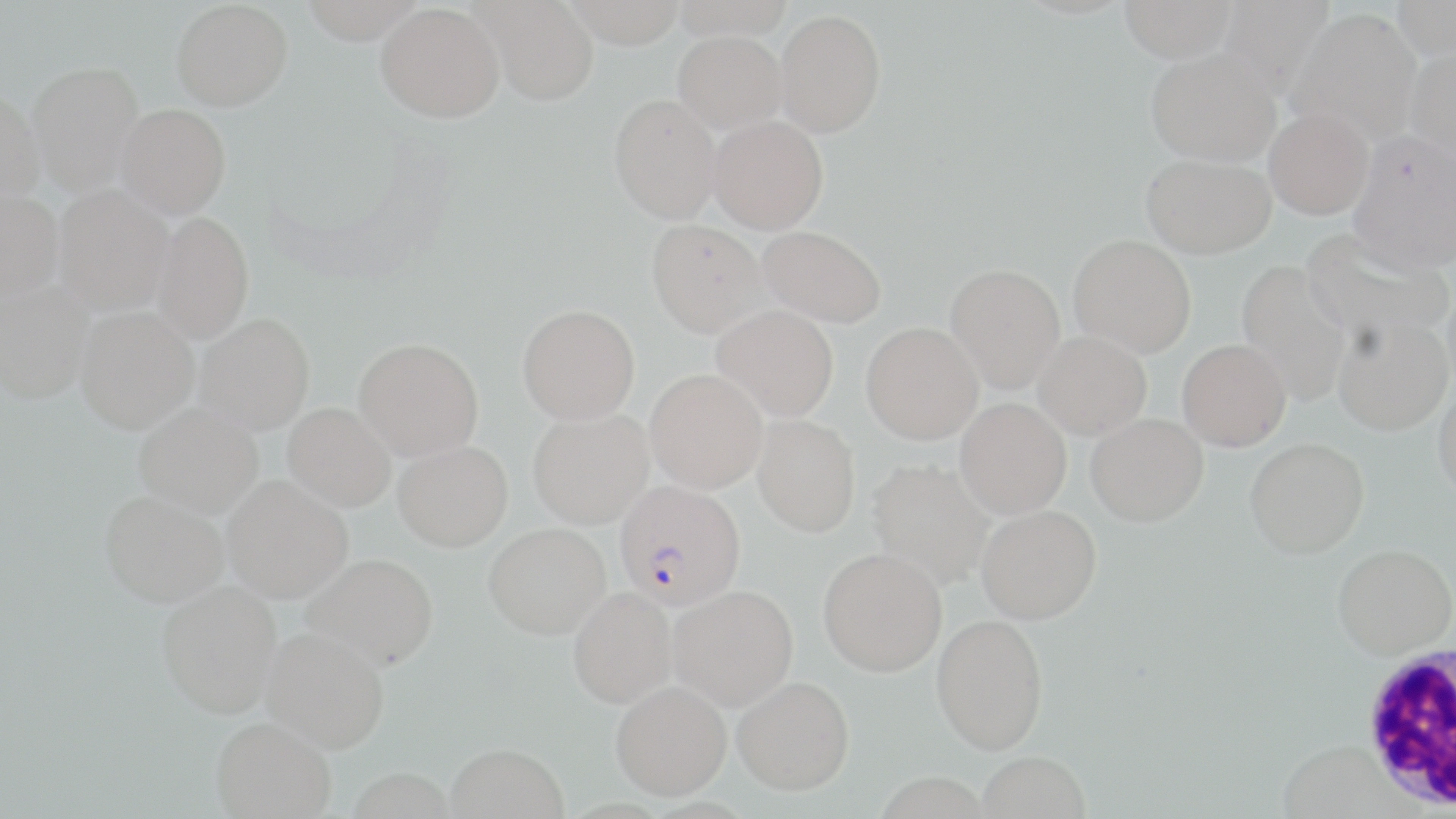
Approximate bounding boxes as (x1, y1, x2, y2) in pixels. Plasmodium falciparum-infected red blood cell locations: (615, 483, 746, 614). Uninfected red blood cell locations: (171, 0, 292, 110), (299, 0, 426, 44), (471, 0, 599, 106), (561, 0, 686, 48), (671, 0, 794, 40), (1119, 0, 1236, 63), (1216, 0, 1336, 100), (1392, 0, 1456, 61), (375, 2, 504, 122), (775, 8, 886, 138), (1287, 9, 1421, 145), (674, 30, 787, 134), (1407, 43, 1456, 175), (1146, 48, 1279, 166), (27, 60, 145, 195), (0, 90, 45, 209), (609, 93, 722, 223), (116, 103, 231, 220), (1264, 108, 1373, 219), (708, 115, 828, 234), (1348, 130, 1456, 274), (1141, 153, 1275, 258), (53, 188, 175, 320), (0, 192, 64, 307), (151, 213, 254, 347), (646, 219, 767, 337), (757, 225, 886, 327), (1300, 229, 1453, 348), (1068, 234, 1196, 357), (1236, 260, 1352, 406), (945, 264, 1067, 393), (0, 283, 94, 408), (712, 305, 839, 421), (517, 306, 640, 426), (75, 310, 199, 439), (1333, 314, 1453, 436), (194, 316, 315, 438), (861, 322, 983, 444), (1033, 330, 1152, 439), (1177, 339, 1291, 451), (353, 340, 484, 463), (645, 370, 768, 495), (1432, 382, 1456, 502), (955, 397, 1071, 520), (282, 405, 395, 515), (133, 407, 263, 523), (527, 411, 654, 532), (1085, 413, 1208, 527), (752, 415, 861, 537), (1244, 437, 1369, 559), (392, 445, 513, 557), (867, 459, 995, 590), (222, 480, 353, 608), (99, 496, 228, 613), (976, 505, 1101, 625), (483, 526, 610, 643), (1332, 543, 1456, 660), (818, 549, 947, 678), (302, 558, 439, 677), (156, 585, 282, 723), (669, 587, 799, 712), (568, 590, 676, 711), (931, 615, 1049, 755), (261, 633, 388, 758), (732, 677, 854, 798), (611, 684, 732, 803), (210, 721, 335, 819), (444, 747, 568, 819), (977, 751, 1091, 819), (346, 771, 455, 819). White blood cell locations: (1357, 643, 1456, 813). Slide-level diagnosis: Plasmodium falciparum. 1000x magnification. May-Grünwald-Giemsa-stained preparation. Single field of view. Thin blood smear. Image is 1456×819 pixels. Light microscopy.